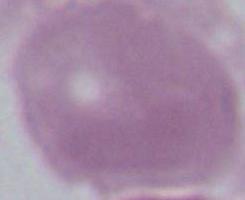

magnification: 1000x
identification: red blood cell
modality: micrograph